Outline each uninfected red blood cell.
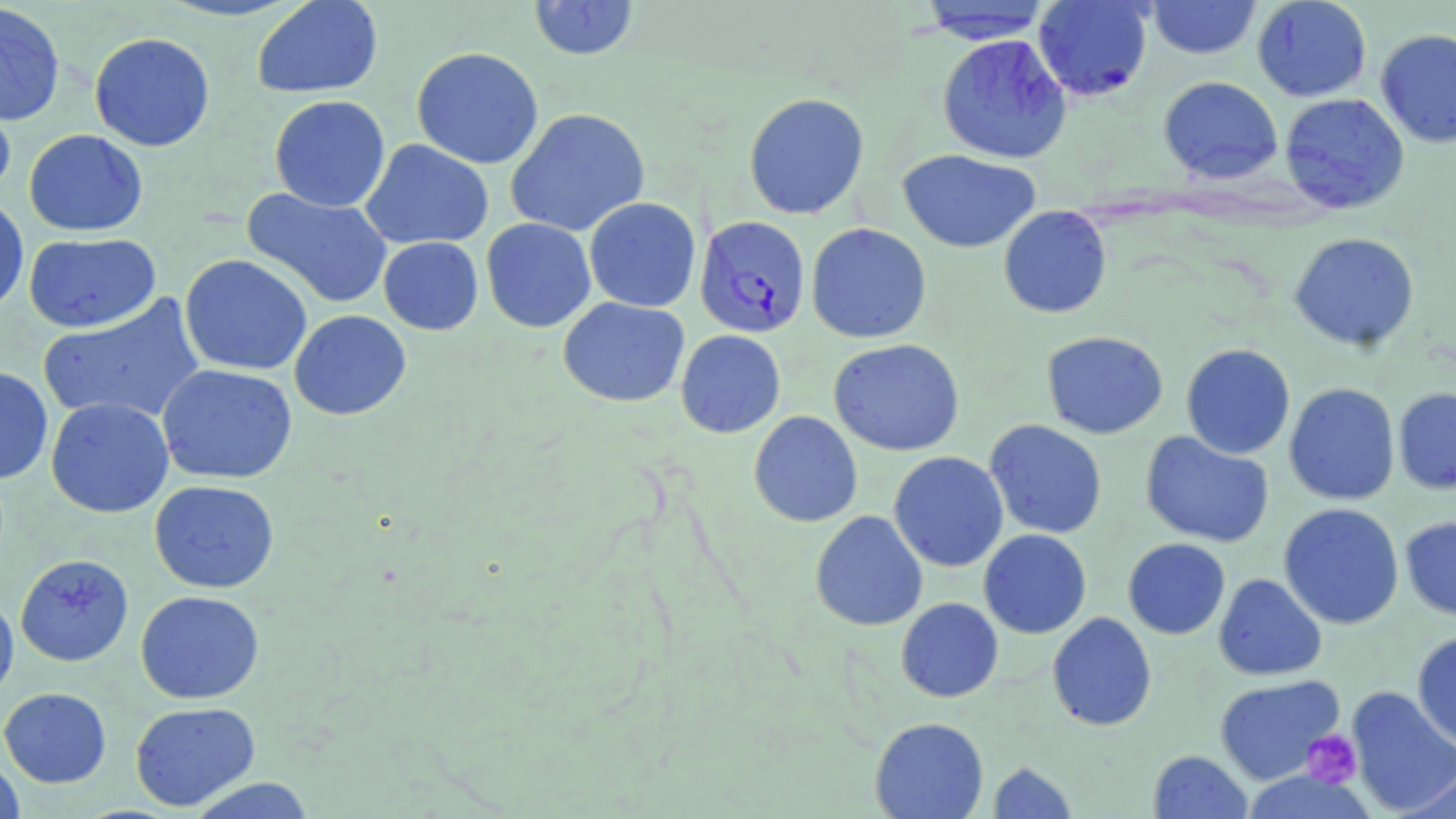

Approximate bounding boxes as (x1, y1, x2, y2) in pixels.
Uninfected red blood cells: (251, 0, 384, 99), (528, 0, 640, 60), (1033, 0, 1153, 101), (1146, 0, 1262, 59), (1252, 0, 1372, 102), (915, 1, 1056, 44), (0, 3, 66, 127), (1375, 28, 1456, 149), (89, 32, 215, 152), (936, 33, 1072, 164), (411, 46, 544, 169), (1158, 76, 1283, 184), (0, 88, 17, 204), (743, 92, 870, 220), (1279, 93, 1410, 214), (269, 95, 391, 212), (505, 107, 650, 237), (24, 129, 148, 236), (360, 139, 494, 250), (897, 149, 1041, 253), (241, 188, 392, 309), (0, 195, 29, 315), (584, 197, 702, 312), (998, 205, 1112, 318), (481, 218, 596, 333), (805, 223, 932, 344), (23, 232, 161, 333), (1288, 232, 1420, 351), (378, 237, 483, 335), (179, 254, 312, 376), (39, 293, 206, 428), (558, 297, 690, 407), (289, 310, 412, 420), (675, 329, 785, 438), (1041, 331, 1168, 439), (828, 338, 965, 456), (1180, 343, 1296, 460), (156, 363, 298, 484), (0, 366, 54, 485), (1283, 383, 1400, 505), (1393, 387, 1456, 494), (45, 397, 174, 518), (748, 410, 863, 527), (984, 419, 1107, 539), (1140, 431, 1274, 548), (888, 451, 1009, 572), (149, 480, 280, 593), (1278, 503, 1405, 630), (810, 510, 927, 631), (1400, 515, 1456, 621), (978, 529, 1092, 639), (1123, 538, 1230, 639), (15, 554, 134, 667), (1213, 573, 1327, 681), (135, 590, 265, 704), (0, 592, 19, 705), (895, 597, 1003, 702), (1046, 612, 1157, 732), (1412, 631, 1456, 752), (1214, 675, 1345, 784), (1345, 686, 1456, 817), (0, 687, 112, 787), (130, 701, 261, 811), (869, 717, 989, 818), (1148, 750, 1252, 819), (0, 755, 25, 819), (987, 762, 1077, 818), (1400, 764, 1456, 819), (1239, 770, 1376, 819), (186, 777, 317, 818).

Summary:
  - Plasmodium falciparum-infected red blood cell locations: (694, 216, 811, 338)
  - Platelet locations: (1302, 729, 1363, 788)
  - Slide-level diagnosis: Plasmodium falciparum
  - Image size: 1456×819 pixels
  - Stain: May-Grünwald-Giemsa
  - Modality: optical microscopy
  - Preparation: thin blood film
  - Field of view: single
  - Magnification: 1000x